State which parasite is depicted.
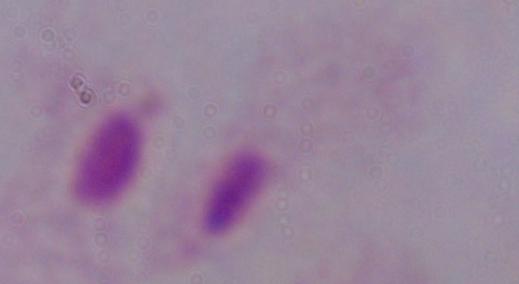
A trichomonad.

Photomicrograph. Captured at 1000x magnification.